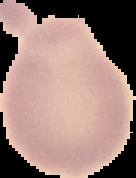

image type = segmented cell region on a black background
preparation = thin blood film
malaria status = uninfected
image size = 136×178 pixels